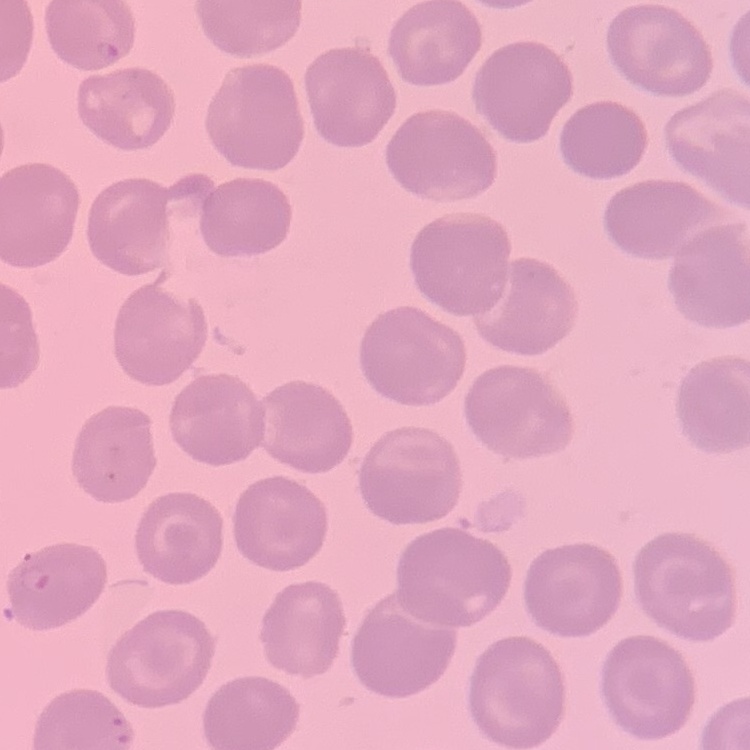

The erythrocytes show no rouleaux formation. Field's or Giemsa stain. Thin blood film. Square crop of a larger photomicrograph.